Outline each blood parasite and name the species.
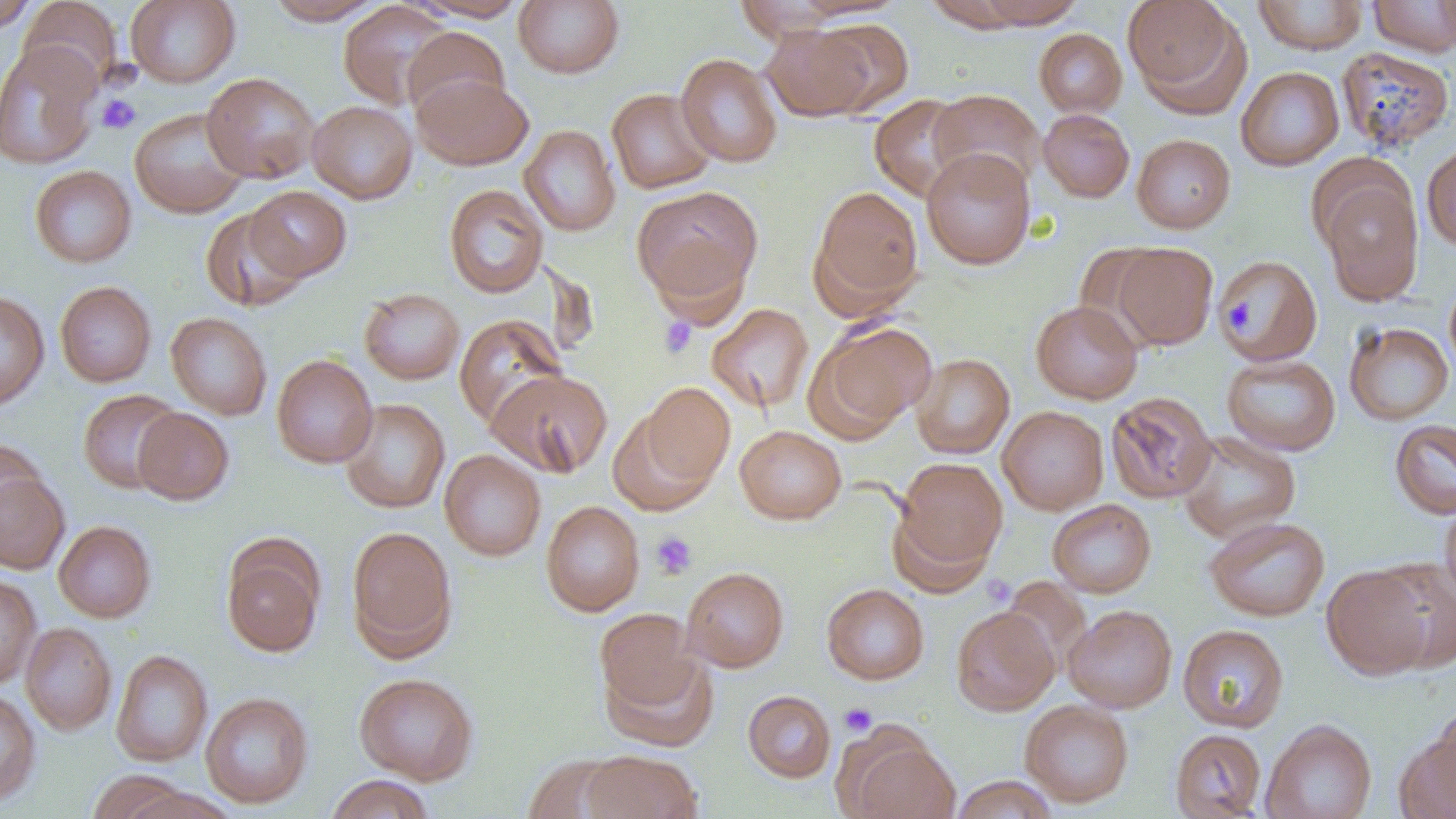
No blood parasites seen.

Approximate bounding boxes as (x1, y1, x2, y2) in pixels. Uninfected red blood cell locations: (0, 0, 39, 33), (126, 0, 241, 88), (264, 0, 386, 25), (412, 0, 529, 21), (513, 0, 625, 78), (791, 0, 906, 20), (975, 0, 1085, 28), (1124, 0, 1242, 105), (1253, 0, 1367, 54), (1368, 0, 1456, 57), (1437, 0, 1456, 50), (18, 1, 124, 94), (337, 1, 456, 110), (733, 1, 846, 41), (923, 1, 1029, 31), (810, 18, 915, 117), (762, 24, 876, 122), (402, 27, 510, 122), (1034, 28, 1127, 116), (0, 41, 101, 170), (1336, 46, 1455, 153), (675, 53, 783, 168), (1236, 66, 1344, 171), (201, 72, 320, 184), (411, 73, 533, 170), (606, 88, 716, 194), (929, 89, 1045, 192), (869, 94, 973, 202), (308, 100, 417, 204), (129, 107, 249, 219), (1038, 108, 1135, 202), (519, 125, 621, 236), (1132, 134, 1236, 233), (1421, 140, 1456, 252), (921, 148, 1036, 270), (29, 165, 137, 268), (1320, 176, 1424, 306), (443, 184, 549, 299), (632, 185, 763, 308), (810, 185, 924, 314), (245, 186, 351, 282), (200, 208, 308, 311), (1073, 242, 1166, 342), (1112, 243, 1218, 349), (1216, 254, 1323, 367), (1444, 274, 1456, 379), (55, 281, 156, 387), (359, 288, 465, 385), (0, 290, 49, 411), (1030, 300, 1143, 404), (707, 303, 814, 413), (166, 312, 272, 420), (453, 314, 568, 429), (810, 321, 938, 436), (1344, 321, 1454, 426), (912, 353, 1015, 458), (1222, 353, 1341, 456), (272, 354, 377, 468), (486, 369, 613, 478), (636, 382, 735, 494), (77, 389, 183, 493), (1105, 391, 1217, 504), (339, 398, 450, 514), (997, 406, 1109, 515), (133, 407, 234, 505), (1390, 418, 1456, 519), (734, 425, 846, 524), (1177, 431, 1301, 542), (0, 439, 45, 536), (439, 449, 546, 561), (893, 457, 1007, 572), (0, 469, 70, 573), (1439, 496, 1456, 605), (1047, 499, 1157, 598), (541, 500, 645, 616), (887, 504, 996, 599), (1204, 516, 1330, 622), (54, 520, 156, 622), (346, 526, 458, 658), (221, 541, 324, 657), (1370, 556, 1456, 674), (1322, 565, 1434, 680), (681, 566, 789, 672), (0, 575, 41, 690), (822, 583, 929, 684), (1063, 604, 1177, 713), (951, 607, 1059, 716), (595, 608, 704, 714), (21, 623, 117, 735), (1178, 624, 1289, 733), (602, 647, 718, 752), (111, 649, 213, 767), (354, 672, 478, 785), (0, 688, 41, 808), (743, 690, 836, 782), (200, 691, 313, 808), (1020, 699, 1134, 807), (1428, 700, 1456, 812), (1261, 719, 1377, 819), (1400, 721, 1456, 818), (1169, 728, 1266, 818), (841, 730, 959, 819), (580, 750, 702, 819), (523, 754, 628, 819), (86, 769, 193, 819), (324, 774, 436, 819), (951, 776, 1059, 818), (119, 785, 242, 819). Platelet locations: (97, 94, 141, 134), (1220, 294, 1259, 336), (659, 317, 698, 358), (650, 531, 698, 580), (839, 703, 877, 736). Slide-level diagnosis: no evidence of blood parasites. One field of a larger specimen. Optical microscopy. Image is 1456×819 pixels. 1000x magnification. Thin blood smear.